Give the extent of all Plasmodium falciparum-infected red blood cells.
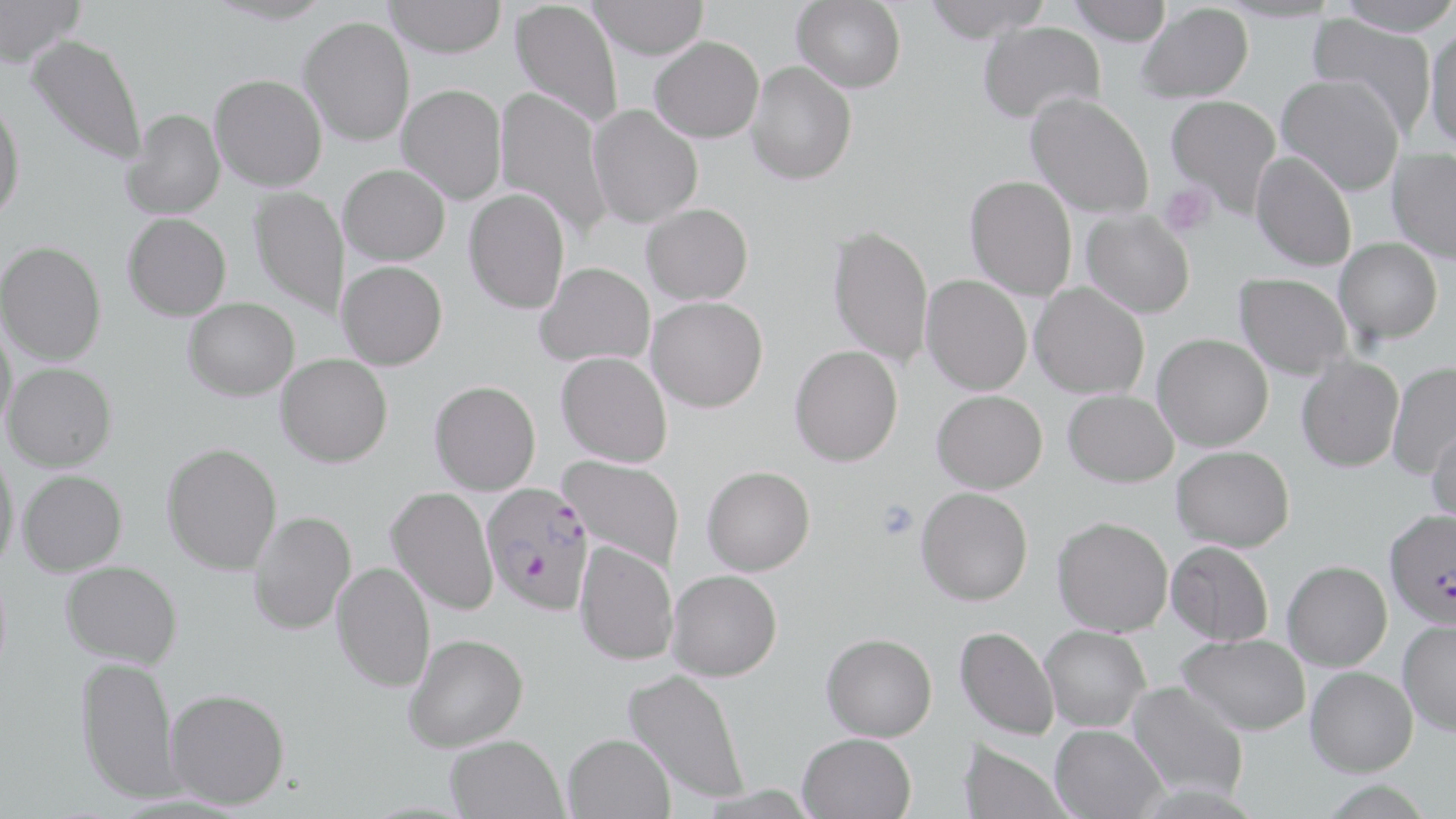

Approximate bounding boxes as named x1/y1/x2/y2 corners in pixels.
Plasmodium falciparum-infected red blood cells: (x1=481, y1=482, x2=594, y2=615), (x1=1384, y1=508, x2=1456, y2=628).

Platelet locations: (x1=1159, y1=183, x2=1218, y2=237), (x1=875, y1=500, x2=919, y2=538). Uninfected red blood cell locations: (x1=383, y1=0, x2=508, y2=57), (x1=588, y1=0, x2=708, y2=59), (x1=792, y1=0, x2=907, y2=92), (x1=921, y1=0, x2=1052, y2=42), (x1=1066, y1=0, x2=1173, y2=45), (x1=1335, y1=0, x2=1456, y2=36), (x1=0, y1=1, x2=83, y2=64), (x1=510, y1=1, x2=624, y2=129), (x1=1136, y1=3, x2=1253, y2=102), (x1=1307, y1=13, x2=1438, y2=136), (x1=300, y1=16, x2=415, y2=146), (x1=978, y1=21, x2=1105, y2=125), (x1=1425, y1=27, x2=1456, y2=152), (x1=27, y1=33, x2=147, y2=166), (x1=649, y1=36, x2=764, y2=142), (x1=746, y1=61, x2=857, y2=184), (x1=210, y1=74, x2=327, y2=191), (x1=1277, y1=74, x2=1405, y2=195), (x1=397, y1=84, x2=507, y2=204), (x1=494, y1=87, x2=612, y2=239), (x1=1026, y1=93, x2=1155, y2=219), (x1=0, y1=94, x2=26, y2=222), (x1=1166, y1=94, x2=1281, y2=214), (x1=587, y1=104, x2=703, y2=228), (x1=122, y1=108, x2=225, y2=220), (x1=1387, y1=148, x2=1456, y2=263), (x1=1251, y1=151, x2=1357, y2=271), (x1=339, y1=163, x2=450, y2=264), (x1=965, y1=175, x2=1077, y2=301), (x1=248, y1=186, x2=349, y2=320), (x1=464, y1=188, x2=570, y2=314), (x1=642, y1=203, x2=753, y2=304), (x1=1081, y1=209, x2=1195, y2=318), (x1=123, y1=212, x2=231, y2=321), (x1=827, y1=222, x2=934, y2=367), (x1=1335, y1=238, x2=1442, y2=344), (x1=1, y1=240, x2=106, y2=365), (x1=337, y1=261, x2=448, y2=369), (x1=535, y1=261, x2=655, y2=368), (x1=1235, y1=272, x2=1352, y2=379), (x1=921, y1=275, x2=1032, y2=395), (x1=1030, y1=283, x2=1150, y2=399), (x1=646, y1=296, x2=768, y2=412), (x1=184, y1=297, x2=300, y2=400), (x1=0, y1=319, x2=18, y2=438), (x1=1153, y1=333, x2=1273, y2=451), (x1=789, y1=344, x2=903, y2=466), (x1=556, y1=352, x2=672, y2=467), (x1=276, y1=354, x2=393, y2=467), (x1=1296, y1=356, x2=1404, y2=472), (x1=1386, y1=362, x2=1456, y2=480), (x1=4, y1=363, x2=117, y2=471), (x1=429, y1=380, x2=541, y2=494), (x1=1063, y1=389, x2=1178, y2=487), (x1=932, y1=390, x2=1047, y2=493), (x1=1426, y1=419, x2=1456, y2=525), (x1=162, y1=442, x2=282, y2=575), (x1=1172, y1=445, x2=1295, y2=551), (x1=0, y1=448, x2=20, y2=574), (x1=559, y1=455, x2=685, y2=572), (x1=702, y1=465, x2=815, y2=575), (x1=18, y1=470, x2=127, y2=576), (x1=387, y1=486, x2=498, y2=615), (x1=916, y1=487, x2=1033, y2=605), (x1=248, y1=510, x2=356, y2=635), (x1=1052, y1=516, x2=1173, y2=636), (x1=574, y1=540, x2=678, y2=666), (x1=1166, y1=541, x2=1273, y2=645), (x1=1282, y1=560, x2=1392, y2=671), (x1=60, y1=561, x2=182, y2=669), (x1=332, y1=561, x2=435, y2=692), (x1=667, y1=569, x2=782, y2=681), (x1=1399, y1=619, x2=1456, y2=735), (x1=1040, y1=624, x2=1151, y2=731), (x1=955, y1=626, x2=1059, y2=740), (x1=822, y1=632, x2=937, y2=741), (x1=404, y1=633, x2=528, y2=751), (x1=1178, y1=633, x2=1310, y2=735), (x1=75, y1=653, x2=183, y2=805), (x1=1305, y1=666, x2=1417, y2=776), (x1=624, y1=670, x2=750, y2=803), (x1=1126, y1=681, x2=1248, y2=800), (x1=165, y1=688, x2=290, y2=809), (x1=1050, y1=724, x2=1167, y2=819), (x1=797, y1=732, x2=916, y2=819), (x1=563, y1=733, x2=675, y2=819), (x1=445, y1=734, x2=568, y2=819), (x1=958, y1=738, x2=1072, y2=819). Slide-level diagnosis: Plasmodium falciparum. Light microscopy. One field of a larger specimen. May-Grünwald-Giemsa stain. Image is 1456×819 pixels. Thin blood smear. Captured at 1000x magnification.